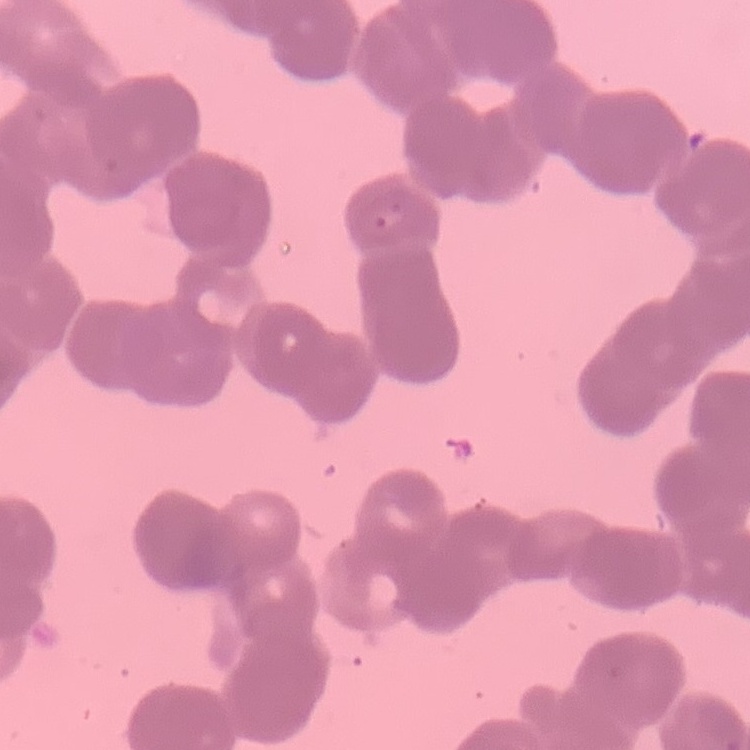

{
  "erythrocyte_morphology": "rouleaux formation",
  "preparation": "thin peripheral smear",
  "image_type": "square crop of a larger photomicrograph",
  "stain": "Field's or Giemsa"
}